Point out each Plasmodium parasite.
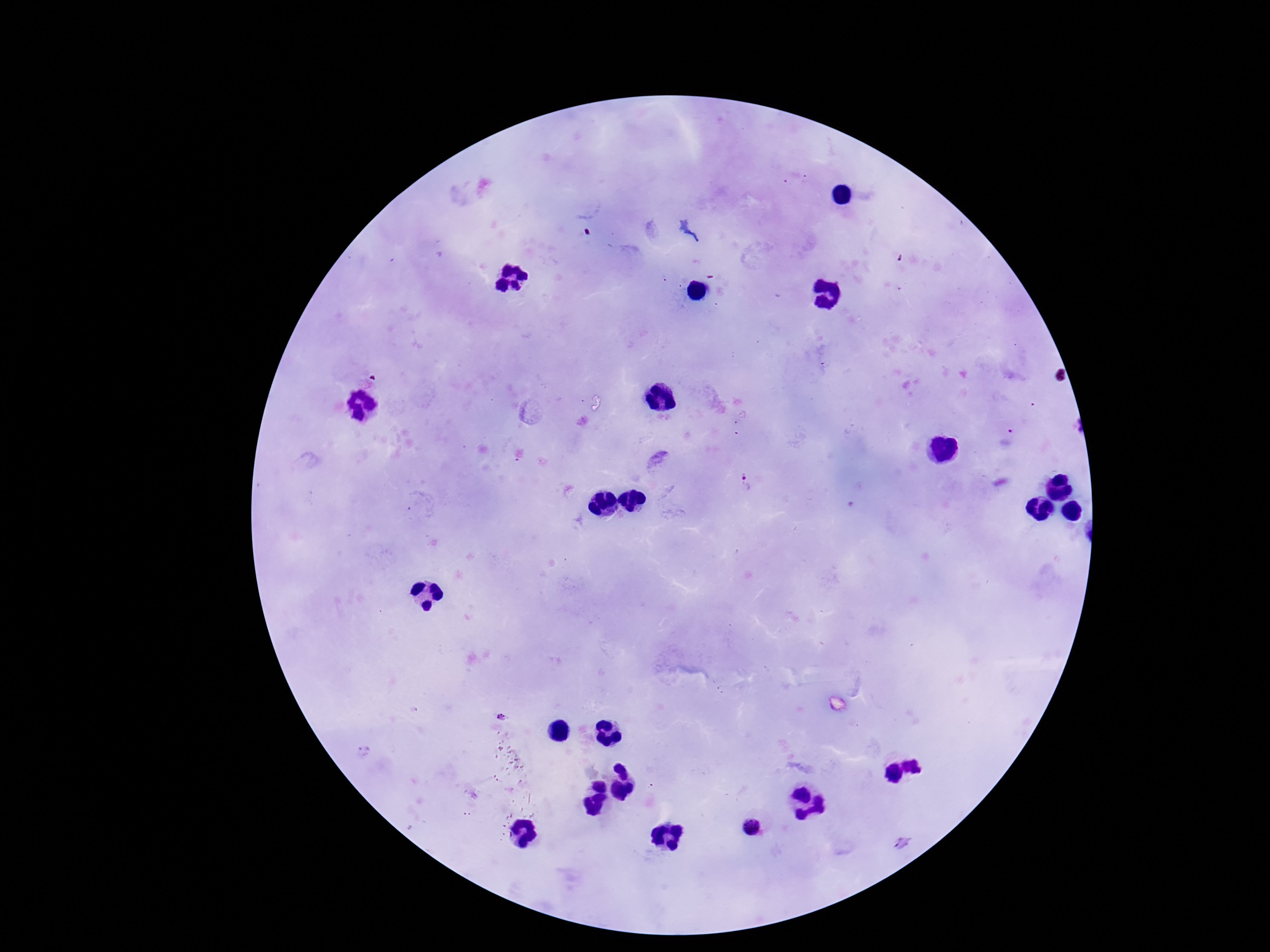
Approximate centers as {x, y} in pixels.
Plasmodium parasites: {747, 482}, {502, 717}, {753, 828}.

Photographed through the microscope eyepiece with a smartphone camera. Patient malaria status: positive. Image is 1270×952 pixels. One field from this slide. 100x magnification. Thick blood smear. Giemsa-stained preparation.